State which cell type is depicted.
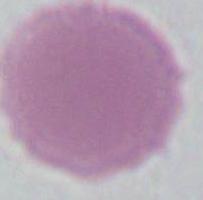
An erythrocyte.

Captured at 1000x magnification. Photomicrograph.